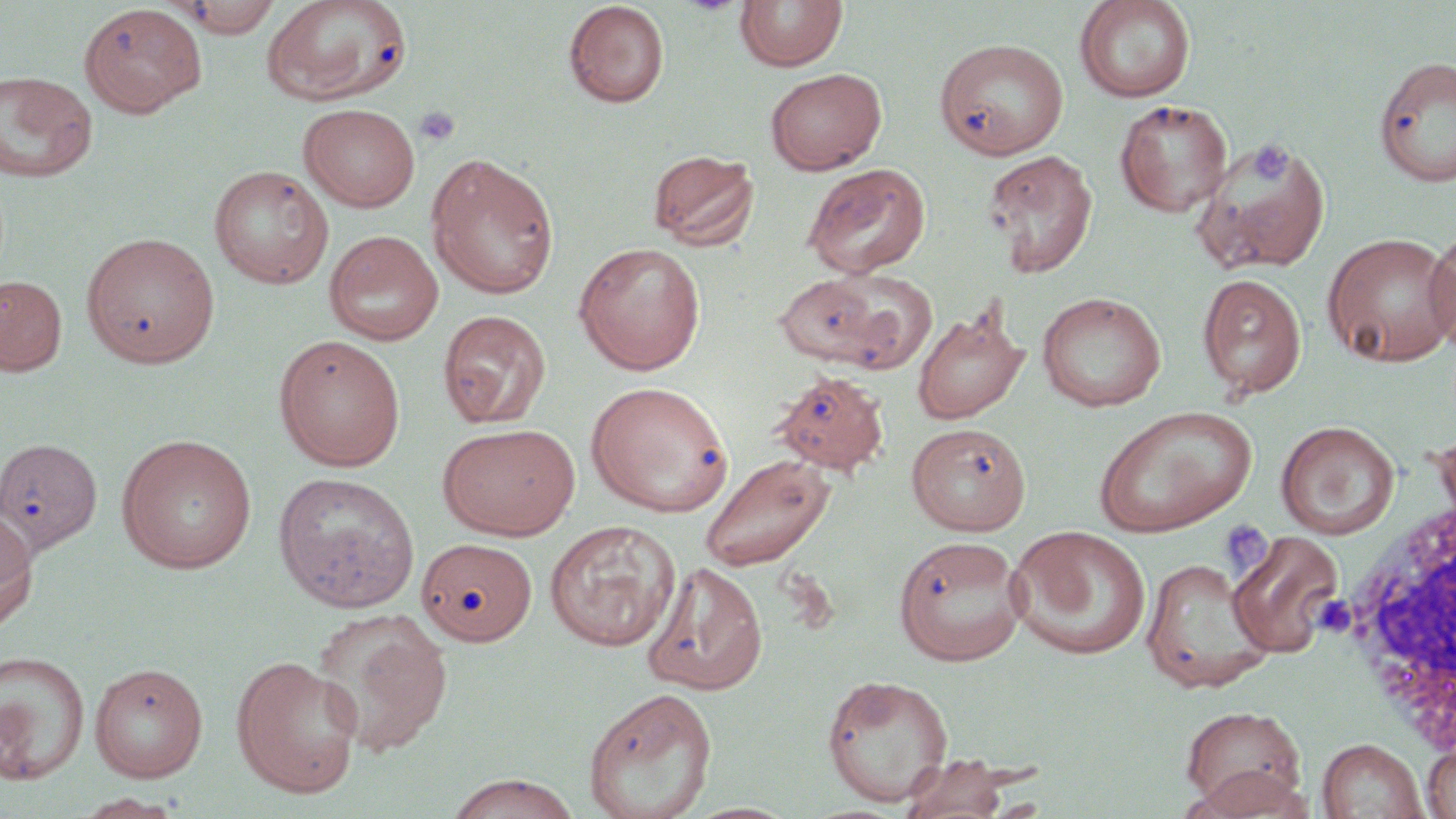

Approximate bounding boxes as (x1, y1, x2, y2) in pixels. White blood cell locations: (1333, 495, 1456, 759). Uninfected red blood cell locations: (173, 0, 284, 38), (261, 0, 414, 106), (1074, 0, 1196, 102), (563, 1, 670, 109), (734, 1, 848, 72), (79, 4, 207, 116), (934, 37, 1069, 160), (1374, 56, 1456, 187), (764, 67, 887, 175), (0, 70, 99, 183), (1114, 99, 1233, 217), (298, 102, 421, 213), (1193, 134, 1332, 275), (648, 148, 760, 251), (983, 148, 1099, 278), (425, 152, 560, 299), (802, 162, 931, 279), (208, 165, 334, 288), (1425, 225, 1456, 358), (324, 230, 444, 346), (1321, 231, 1456, 366), (80, 232, 220, 368), (573, 241, 706, 375), (826, 270, 938, 375), (1196, 273, 1307, 400), (1, 274, 68, 376), (773, 274, 883, 367), (1037, 291, 1166, 411), (911, 303, 1030, 424), (438, 310, 552, 429), (273, 334, 406, 471), (771, 369, 890, 475), (586, 380, 733, 516), (1094, 405, 1257, 537), (1277, 421, 1399, 540), (437, 422, 580, 540), (906, 422, 1031, 536), (115, 433, 257, 574), (0, 437, 103, 557), (697, 452, 836, 573), (272, 472, 419, 613), (0, 513, 36, 636), (545, 519, 680, 651), (1007, 525, 1151, 660), (1226, 530, 1345, 657), (892, 534, 1028, 666), (417, 538, 538, 646), (1141, 556, 1273, 693), (643, 560, 768, 695), (311, 608, 454, 757), (0, 650, 90, 786), (230, 654, 363, 798), (89, 662, 208, 782), (822, 674, 954, 806), (583, 686, 718, 819), (1180, 704, 1307, 813), (1317, 738, 1426, 818), (1422, 740, 1456, 819), (891, 755, 1021, 818), (1181, 766, 1315, 818), (443, 773, 583, 819), (70, 793, 188, 819). Platelet locations: (414, 106, 461, 147), (1248, 141, 1291, 184), (1220, 519, 1275, 577), (1314, 591, 1362, 640). Slide-level diagnosis: no evidence of blood parasites. Captured at 1000x magnification. One field of a larger specimen. May-Grünwald-Giemsa-stained preparation. Light microscopy. Image is 1456×819 pixels. Thin blood smear.